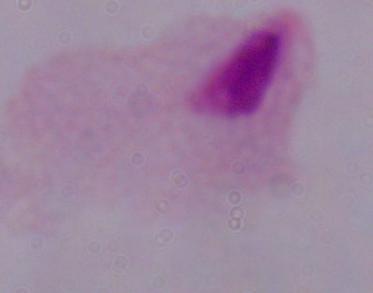 Captured at 1000x magnification. Micrograph. A trichomonad is shown.